Give the position of every leukocyte visible.
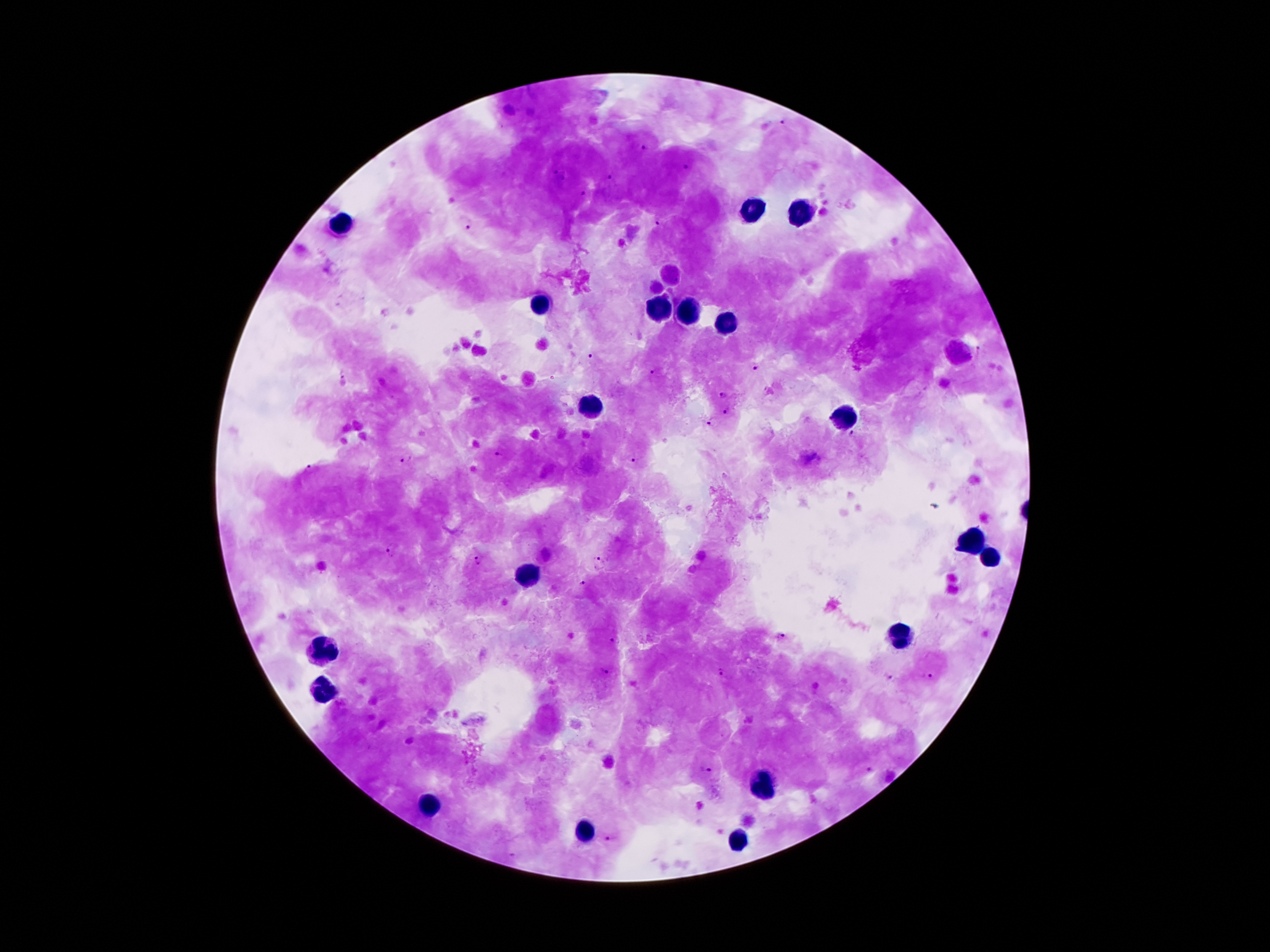

Approximate object centers, in pixels from the top-left corner.
Leukocytes: (x=751, y=208), (x=797, y=212), (x=342, y=223), (x=541, y=305), (x=656, y=309), (x=688, y=309), (x=730, y=321), (x=589, y=407), (x=847, y=416), (x=971, y=538), (x=990, y=559), (x=526, y=575), (x=902, y=635), (x=325, y=650), (x=325, y=691), (x=761, y=784), (x=432, y=804), (x=583, y=832), (x=742, y=840).

Summary:
  - Plasmodium parasite locations: (x=780, y=123), (x=645, y=146), (x=689, y=167), (x=555, y=172), (x=608, y=176), (x=565, y=178), (x=581, y=194), (x=659, y=222), (x=469, y=228), (x=675, y=280), (x=979, y=350), (x=592, y=355), (x=754, y=367), (x=343, y=371), (x=653, y=372), (x=722, y=396), (x=726, y=412), (x=711, y=421), (x=852, y=433), (x=499, y=454), (x=407, y=459), (x=635, y=461), (x=310, y=468), (x=392, y=548), (x=598, y=560), (x=479, y=561), (x=583, y=583), (x=781, y=636), (x=615, y=640), (x=603, y=672), (x=721, y=673), (x=889, y=676), (x=928, y=676), (x=705, y=769), (x=870, y=769), (x=608, y=840)
  - Image size: 1270×952 pixels
  - Capture: smartphone through the microscope eyepiece
  - Preparation: thick blood film
  - Patient malaria status: infected with Plasmodium falciparum
  - Field of view: single
  - Magnification: 100x
  - Stain: Giemsa